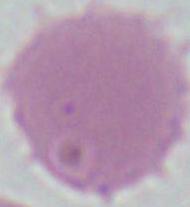

1000x magnification. A red blood cell is shown. Micrograph.